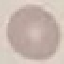

Summary:
  - Malaria status: uninfected
  - Stain: Giemsa
  - Capture: smartphone camera at the microscope eyepiece
  - Preparation: thin blood film
  - Image type: cell patch, automatically extracted from a larger field of view and resized to 64 × 64 pixels